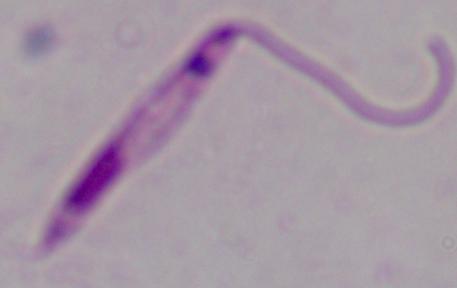

identification = Leishmania
magnification = 1000x
modality = micrograph